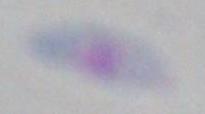

identification = Toxoplasma gondii
magnification = 1000x
modality = micrograph